Classify this cell by malaria status.
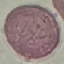
It is uninfected.

image_type: automatically extracted cell patch, resized to 64 × 64 pixels
preparation: thin smear
capture: smartphone through the microscope eyepiece
stain: Giemsa